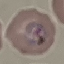
result: malaria parasites detected
preparation: thin blood film
stain: Giemsa
capture: smartphone camera at the microscope eyepiece
image_type: automatically extracted cell patch, resized to 64 × 64 pixels